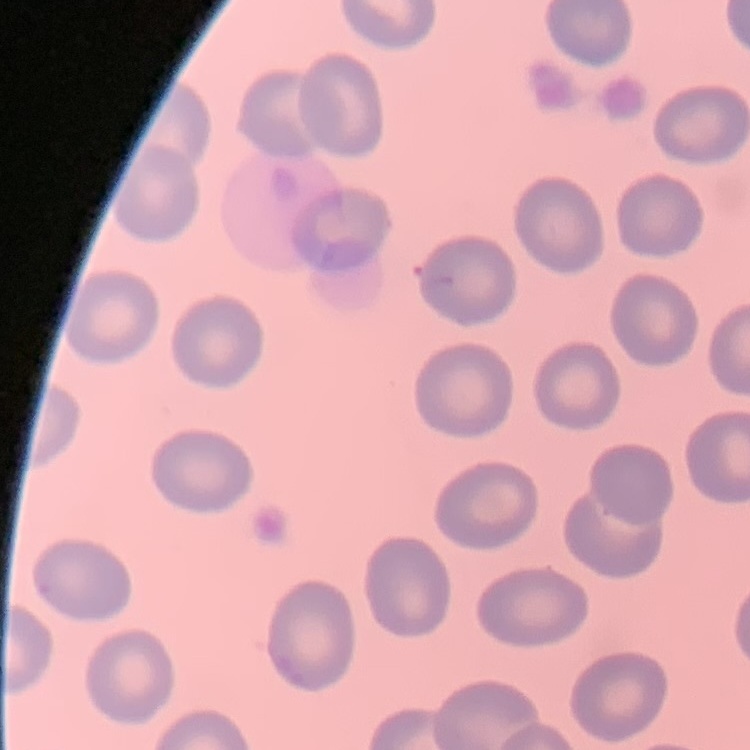

red blood cell morphology = no rouleaux formation
stain = Field's or Giemsa
image type = one tile cut from a larger photomicrograph
preparation = thin peripheral smear